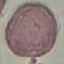
Result: no malaria parasites detected. Thin smear of blood. Automatically extracted cell patch, resized to 64 × 64 pixels. Giemsa-stained preparation. Photographed with a smartphone camera at the microscope eyepiece.